Name the parasite shown.
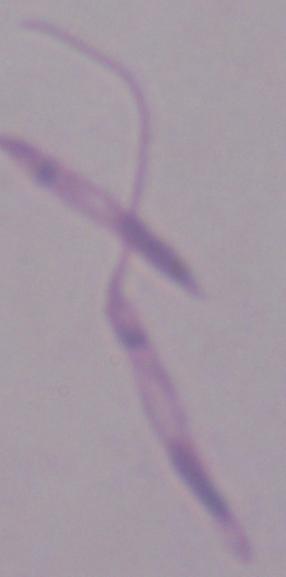

This is Leishmania.

Photomicrograph. Captured at 1000x magnification.